Locate and identify every blood parasite.
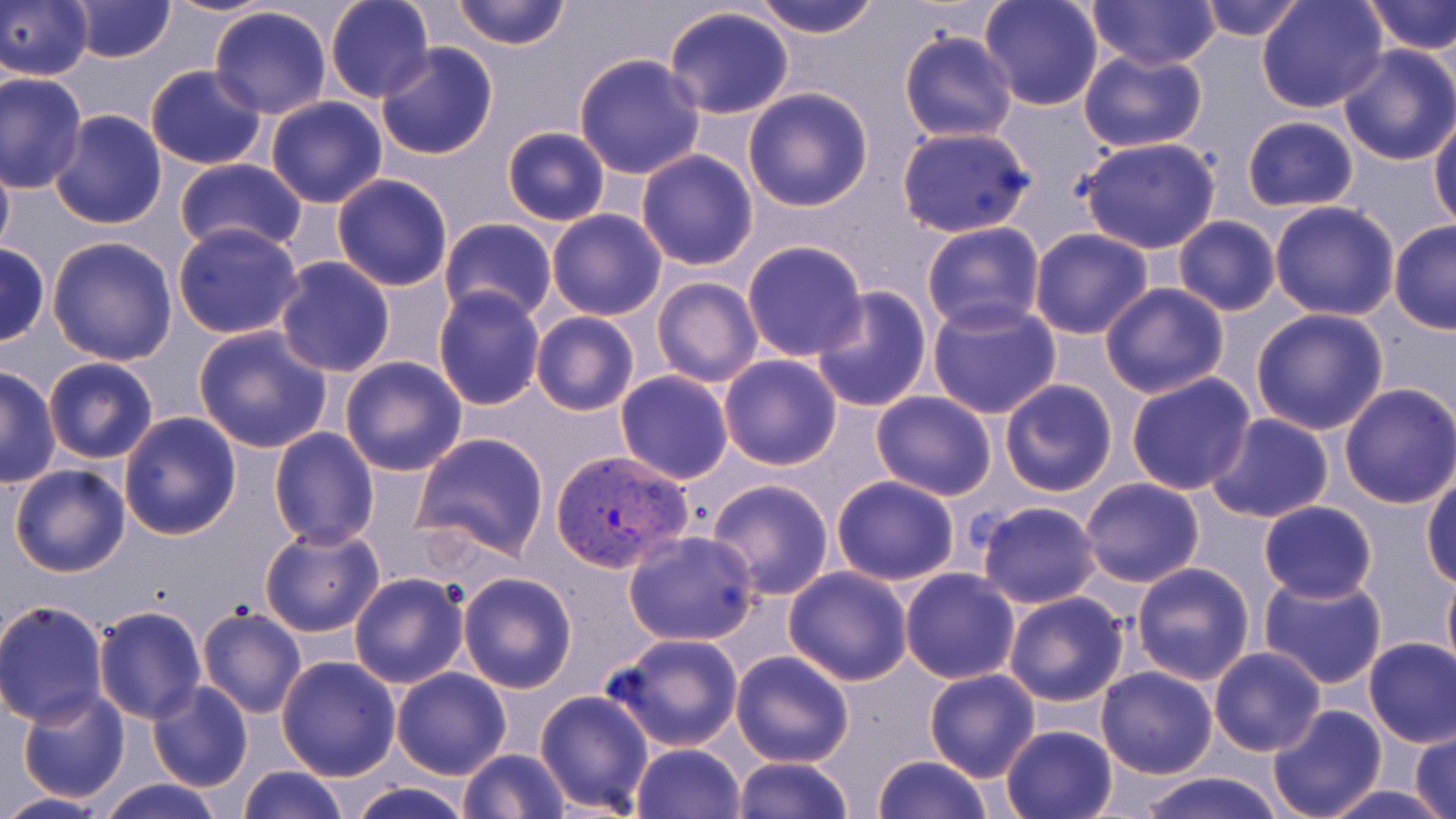
Approximate bounding boxes as (x1,y1)-(x2,y2) corner pairs in pixels.
Plasmodium vivax-infected red blood cells: (551,447)-(694,574).
No Plasmodium falciparum, Plasmodium ovale, Plasmodium malariae, Babesia divergens, or Trypanosoma brucei observed.

{
  "slide_level_diagnosis": "Plasmodium vivax",
  "modality": "light microscopy",
  "field_of_view": "one of a larger specimen",
  "stain": "May-Grünwald-Giemsa",
  "magnification": "1000x",
  "uninfected_red_blood_cell_locations": "approximate bounding boxes as (x1,y1)-(x2,y2) corner pairs in pixels: (66,0)-(176,63), (158,0)-(284,19), (325,0)-(433,102), (449,0)-(570,49), (748,0)-(883,39), (978,0)-(1106,110), (1086,0)-(1220,71), (1194,0)-(1310,41), (1257,0)-(1386,113), (1362,0)-(1455,54), (0,1)-(94,81), (209,6)-(333,119), (662,6)-(794,120), (899,31)-(1016,143), (377,43)-(497,160), (1335,44)-(1456,166), (1078,48)-(1207,152), (573,53)-(707,178), (144,65)-(266,168), (0,71)-(87,193), (741,86)-(874,211), (990,93)-(1105,194), (264,95)-(388,208), (47,109)-(166,229), (1431,113)-(1456,232), (1242,115)-(1359,212), (894,126)-(1035,237), (501,127)-(611,226), (1076,137)-(1222,253), (0,147)-(14,267), (636,150)-(759,271), (175,157)-(306,255), (332,174)-(453,291), (1268,201)-(1399,320), (546,209)-(667,321), (1172,216)-(1280,316), (440,218)-(558,324), (1389,220)-(1456,334), (920,221)-(1046,335), (172,222)-(305,341), (1028,229)-(1153,339), (45,235)-(179,365), (740,239)-(869,362), (0,242)-(50,347), (274,257)-(396,376), (639,274)-(750,481), (651,276)-(763,386), (1099,282)-(1231,399), (809,285)-(932,411), (432,286)-(547,409), (926,297)-(1062,421), (1248,307)-(1391,435), (531,311)-(639,417), (193,325)-(334,454), (719,354)-(843,469), (43,356)-(158,465), (339,356)-(468,476), (0,365)-(60,487), (615,370)-(734,485), (1125,372)-(1257,495), (999,378)-(1118,497), (1338,383)-(1456,509), (870,391)-(997,500), (117,411)-(241,540), (1203,413)-(1334,524), (267,427)-(379,548), (413,432)-(550,560), (9,462)-(131,579), (1422,471)-(1455,588), (830,475)-(960,585), (1079,477)-(1204,588), (705,479)-(835,601), (974,500)-(1104,609), (1257,500)-(1379,602), (259,524)-(384,638), (623,530)-(759,647), (1130,561)-(1255,685), (782,565)-(913,685), (898,567)-(1020,684), (1441,568)-(1456,682), (348,571)-(469,689), (458,572)-(577,693), (1257,572)-(1388,692), (1002,592)-(1129,706), (0,602)-(109,726), (94,605)-(208,723), (197,608)-(307,719), (605,633)-(745,751), (1363,637)-(1456,747), (1208,646)-(1326,757), (729,650)-(855,768), (276,655)-(400,780), (1096,666)-(1219,779), (1225,666)-(1371,804), (391,668)-(511,779), (924,668)-(1041,782), (146,680)-(254,793), (533,689)-(654,812), (17,690)-(130,804), (1266,704)-(1386,819), (1000,724)-(1119,819), (1410,730)-(1456,818), (632,744)-(745,818), (458,748)-(572,819), (872,754)-(993,819), (730,755)-(856,818), (238,765)-(348,819), (1132,773)-(1289,819), (94,777)-(228,819), (346,779)-(473,819), (1322,784)-(1448,818), (0,792)-(118,818)",
  "image_size": "1456×819 pixels",
  "preparation": "thin blood smear"
}